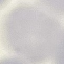

Result: negative for malaria parasites. Thin smear of blood. Automatically extracted cell patch, resized to 64 × 64 pixels. Acquired by smartphone through the microscope eyepiece. Giemsa stain.